Locate every leukocyte (white blood cell).
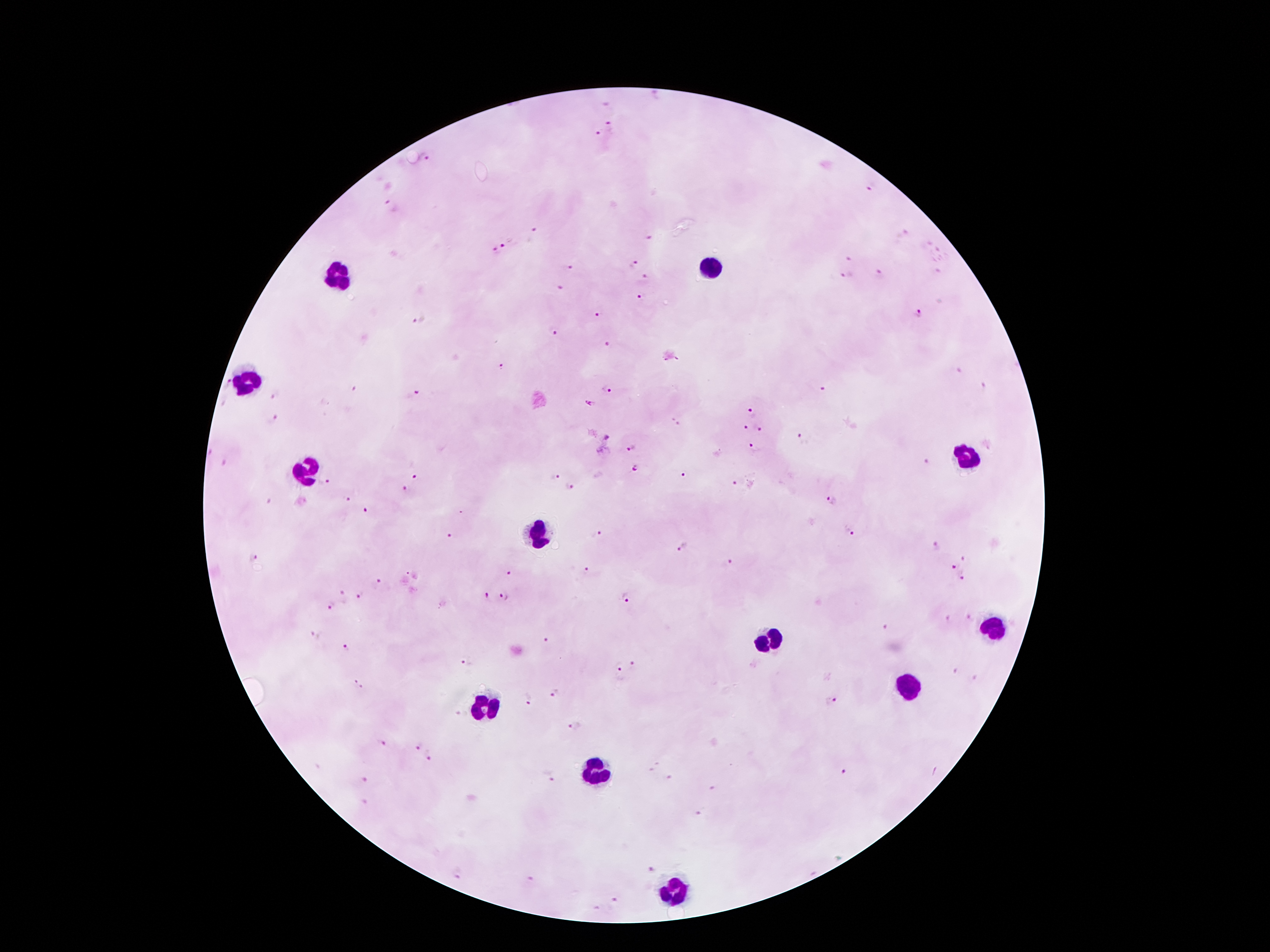

Approximate centers as [x, y] in pixels.
Leukocytes: [712, 268], [341, 275], [246, 384], [967, 456], [306, 471], [538, 535], [993, 631], [770, 641], [905, 685], [483, 706], [595, 771], [675, 889].

Plasmodium parasite locations = [612, 127], [598, 134], [426, 157], [871, 186], [390, 204], [536, 230], [650, 238], [506, 245], [492, 251], [848, 259], [630, 264], [568, 268], [848, 273], [881, 276], [642, 277], [559, 288], [642, 297], [918, 313], [599, 314], [417, 321], [555, 331], [608, 345], [501, 366], [228, 383], [982, 387], [605, 389], [821, 391], [276, 396], [414, 396], [590, 404], [750, 413], [273, 418], [674, 422], [745, 428], [759, 429], [606, 437], [801, 439], [631, 447], [752, 447], [224, 462], [928, 463], [637, 468], [686, 472], [555, 476], [414, 477], [324, 483], [734, 484], [571, 485], [405, 491], [345, 500], [831, 500], [268, 503], [367, 511], [848, 532], [598, 534], [451, 536], [933, 546], [682, 547], [964, 557], [252, 558], [727, 563], [953, 568], [587, 570], [510, 573], [961, 577], [379, 583], [360, 595], [485, 596], [505, 596], [627, 597], [330, 606], [968, 616], [885, 628], [546, 642], [346, 647], [468, 661], [631, 666], [618, 667], [955, 671], [975, 678], [355, 681], [363, 688], [555, 692], [530, 699], [830, 701], [574, 725], [381, 743], [415, 748], [430, 755], [655, 768], [842, 770], [366, 777], [550, 778], [669, 778], [716, 789], [365, 802], [698, 813], [649, 869], [458, 874], [528, 878], [617, 900], [598, 908]
stain = Giemsa
capture = smartphone camera through the microscope eyepiece
magnification = 100x
patient malaria status = positive for Plasmodium falciparum
field of view = one from this slide
image size = 1270×952 pixels
preparation = thick blood film